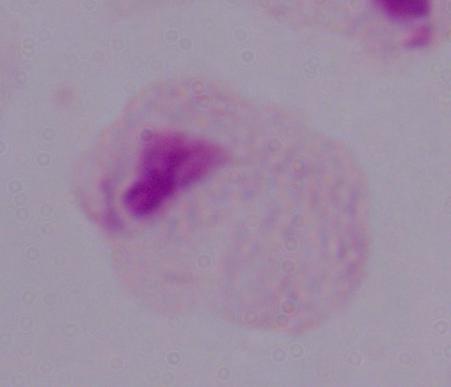
{
  "modality": "micrograph",
  "magnification": "1000x",
  "identification": "trichomonad"
}